Identify the cell.
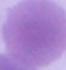
This is an erythrocyte.

Summary:
  - Magnification: 1000x
  - Modality: photomicrograph